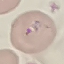
Malaria status: parasitized. Thin blood film. Acquired by smartphone through the microscope eyepiece. Automatically extracted cell patch, resized to 64 × 64 pixels. Giemsa stain.